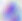
Summary:
  - Identification: Toxoplasma gondii
  - Modality: micrograph
  - Magnification: 400x